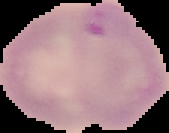

image size = 169×133 pixels
result = Plasmodium parasites detected
image type = segmented cell region on a black background
preparation = thin blood film